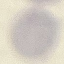

Summary:
  - Result: negative for malaria parasites
  - Capture: smartphone through the microscope eyepiece
  - Image type: cell patch, automatically extracted from a larger field of view and resized to 64 × 64 pixels
  - Stain: Giemsa
  - Preparation: thin blood film